Comment on the morphology of the red blood cells.
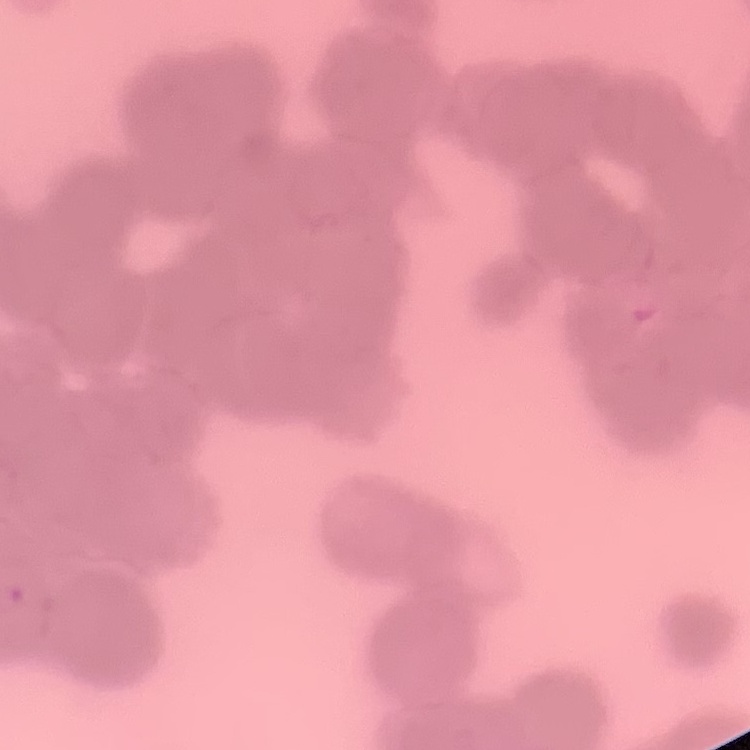

Rouleaux formation.

Stained with either Field's or Giemsa. One tile cut from a larger photomicrograph. Thin peripheral smear.